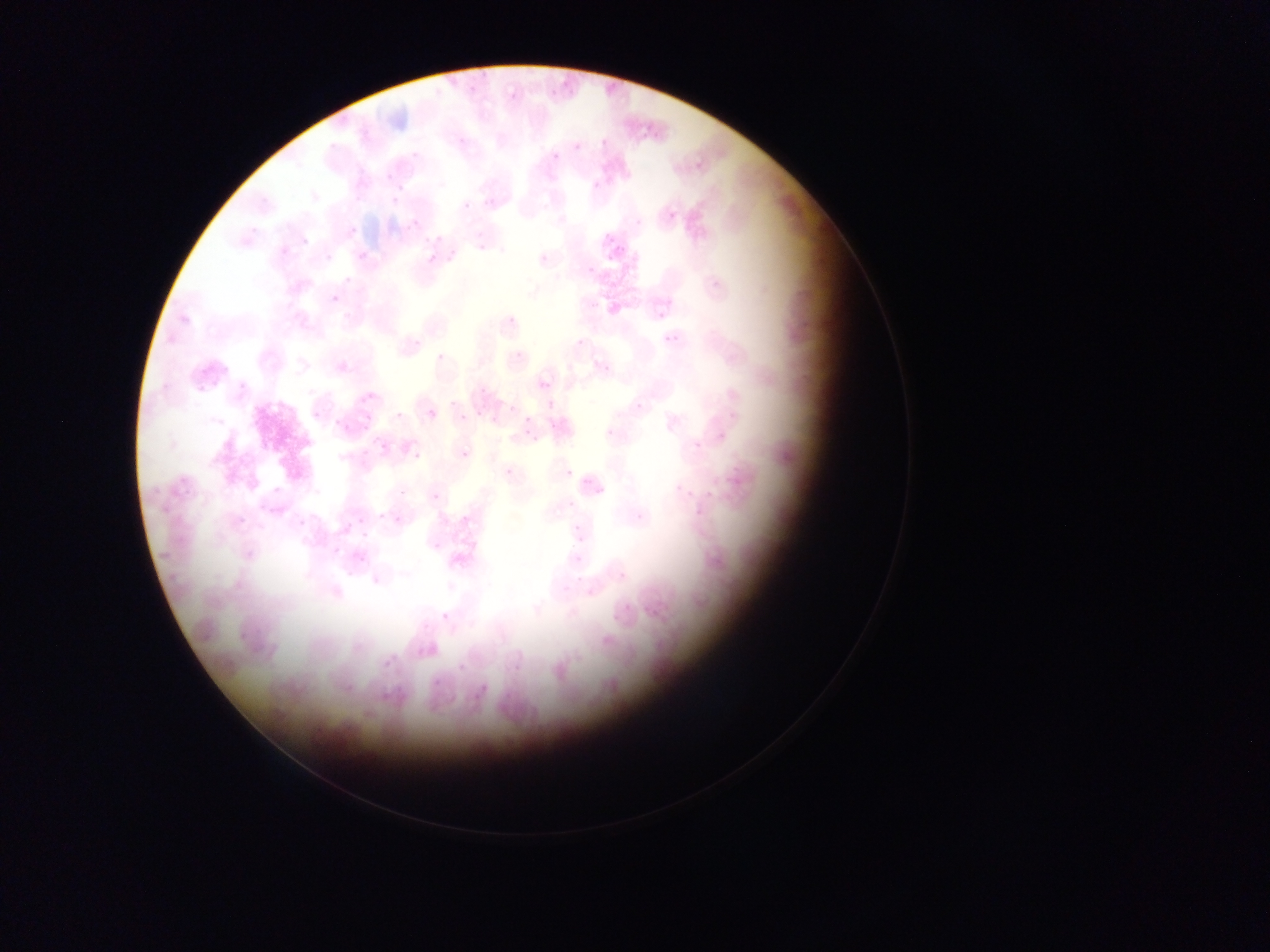 Approximate bounding boxes as [left, top, right, bottom] in pixels. Malaria parasite locations: [386, 171, 394, 182], [395, 183, 404, 192], [392, 195, 398, 205], [667, 211, 676, 220], [410, 218, 419, 225], [349, 226, 358, 235], [604, 232, 615, 243], [615, 244, 627, 254], [358, 249, 368, 262], [427, 252, 438, 263], [323, 253, 329, 263], [587, 265, 595, 271], [331, 293, 341, 304], [673, 335, 680, 343], [540, 381, 551, 389], [360, 395, 368, 403], [510, 405, 520, 410], [428, 411, 437, 416], [365, 415, 373, 420], [549, 417, 558, 429], [335, 419, 341, 427], [345, 424, 356, 428], [363, 426, 371, 429], [525, 430, 533, 436], [372, 436, 381, 447], [383, 443, 387, 452], [359, 446, 370, 459], [565, 468, 574, 478], [583, 478, 595, 487], [271, 484, 282, 496], [568, 501, 575, 509], [380, 511, 386, 519], [238, 516, 246, 527], [393, 516, 401, 522], [299, 517, 307, 527], [346, 519, 354, 528], [572, 526, 582, 531], [361, 529, 369, 539], [578, 534, 587, 544], [333, 543, 338, 556], [575, 554, 585, 563], [359, 558, 368, 563], [383, 660, 392, 668], [458, 663, 466, 674], [433, 676, 440, 690], [481, 680, 488, 692] | approximate [x, y] pixel centers of objects too small to bound: [409, 228], [667, 336], [529, 420], [465, 456], [362, 520]. Collected in Ghana. Single field of view. Image is 1270×952 pixels. Thin blood smear. Photographed through a microscope with a mobile-phone camera.